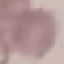
malaria status = uninfected
capture = smartphone through the microscope eyepiece
preparation = thin blood film
stain = Giemsa
image type = cell patch, automatically extracted from a larger field of view and resized to 64 × 64 pixels